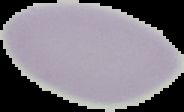
{
  "image_type": "segmented cell region with the area outside set to black",
  "preparation": "thin blood smear",
  "image_size": "184×112 pixels",
  "malaria_status": "uninfected"
}